Point out each leukocyte.
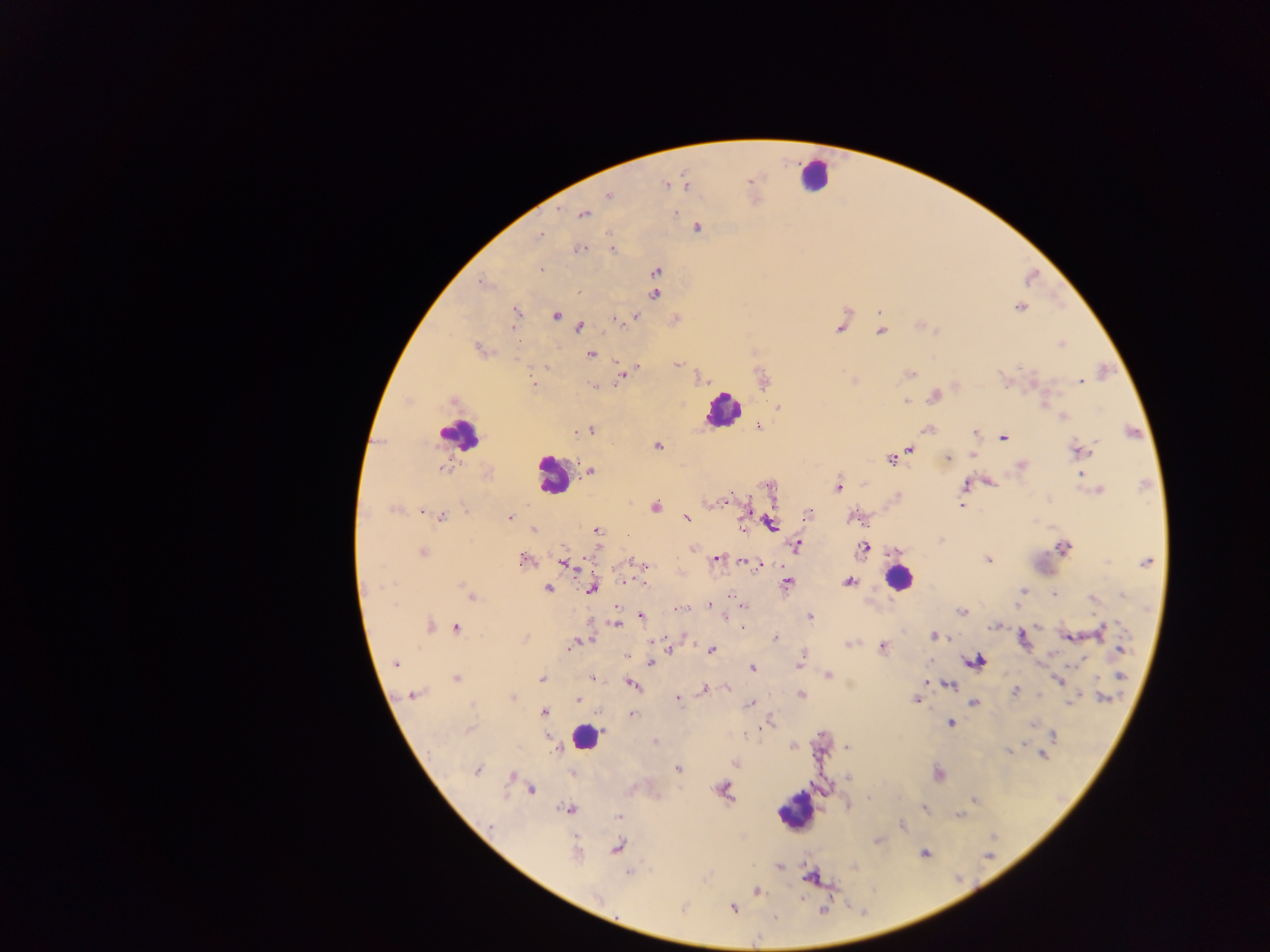
Approximate centers as {x, y} in pixels.
Leukocytes: {818, 179}, {727, 409}, {461, 433}, {553, 476}, {898, 577}, {584, 741}, {797, 810}.

country: Ghana
preparation: thick blood film
field_of_view: single
malaria_parasite_locations: 'approximate centers as {x, y} in pixels: {751, 182}, {666, 185}, {687, 186}, {607, 195}, {559, 210}, {677, 212}, {584, 215}, {698, 226}, {541, 235}, {578, 248}, {610, 249}, {540, 268}, {657, 271}, {481, 282}, {579, 292}, {656, 294}, {1019, 309}, {516, 313}, {556, 315}, {638, 315}, {676, 317}, {615, 319}, {619, 323}, {578, 326}, {837, 328}, {879, 331}, {478, 347}, {1059, 347}, {592, 354}, {677, 364}, {638, 367}, {546, 368}, {528, 374}, {911, 374}, {622, 376}, {851, 379}, {532, 381}, {1081, 381}, {853, 382}, {594, 386}, {935, 396}, {409, 400}, {906, 402}, {1062, 416}, {975, 433}, {1003, 439}, {1097, 441}, {658, 444}, {1093, 446}, {911, 450}, {1087, 451}, {1078, 452}, {971, 456}, {946, 457}, {890, 461}, {1022, 464}, {591, 470}, {443, 471}, {1081, 473}, {989, 480}, {965, 482}, {838, 486}, {1101, 489}, {714, 502}, {723, 502}, {962, 504}, {655, 505}, {393, 511}, {422, 512}, {808, 513}, {442, 516}, {511, 517}, {687, 519}, {853, 520}, {742, 522}, {770, 525}, {533, 527}, {596, 530}, {868, 545}, {799, 546}, {1064, 547}, {424, 551}, {864, 554}, {716, 559}, {627, 560}, {988, 560}, {521, 561}, {560, 561}, {1147, 562}, {564, 564}, {744, 564}, {646, 567}, {754, 567}, {460, 582}, {624, 582}, {849, 582}, {385, 584}, {643, 584}, {787, 584}, {549, 589}, {592, 589}, {1022, 592}, {731, 594}, {1052, 595}, {1121, 596}, {471, 599}, {1091, 600}, {707, 606}, {1015, 606}, {677, 608}, {744, 608}, {961, 611}, {641, 615}, {809, 615}, {1103, 623}, {432, 625}, {615, 625}, {988, 626}, {458, 627}, {741, 628}, {932, 636}, {687, 637}, {590, 638}, {775, 638}, {526, 639}, {654, 642}, {849, 644}, {570, 645}, {883, 646}, {1119, 648}, {671, 650}, {711, 650}, {802, 653}, {627, 656}, {801, 660}, {979, 661}, {395, 663}, {651, 663}, {970, 663}, {798, 664}, {752, 669}, {829, 674}, {1120, 677}, {456, 678}, {544, 678}, {591, 678}, {1057, 680}, {925, 682}, {629, 683}, {950, 684}, {633, 686}, {726, 687}, {703, 690}, {1014, 691}, {801, 693}, {412, 694}, {1038, 695}, {511, 696}, {1102, 697}, {677, 698}, {577, 700}, {915, 701}, {973, 703}, {750, 704}, {544, 711}, {631, 712}, {772, 719}, {950, 724}, {757, 728}, {745, 734}, {1053, 736}, {654, 740}, {791, 746}, {556, 750}, {736, 764}, {479, 770}, {677, 770}, {510, 775}, {531, 789}, {724, 789}, {924, 808}, {567, 810}, {901, 826}, {575, 839}, {617, 847}, {924, 853}, {628, 872}, {757, 892}, {735, 909}, {685, 910}, {775, 917}'
capture: mobile-phone photograph through a microscope
image_size: 1270×952 pixels